Locate every blood parasite and identify its species.
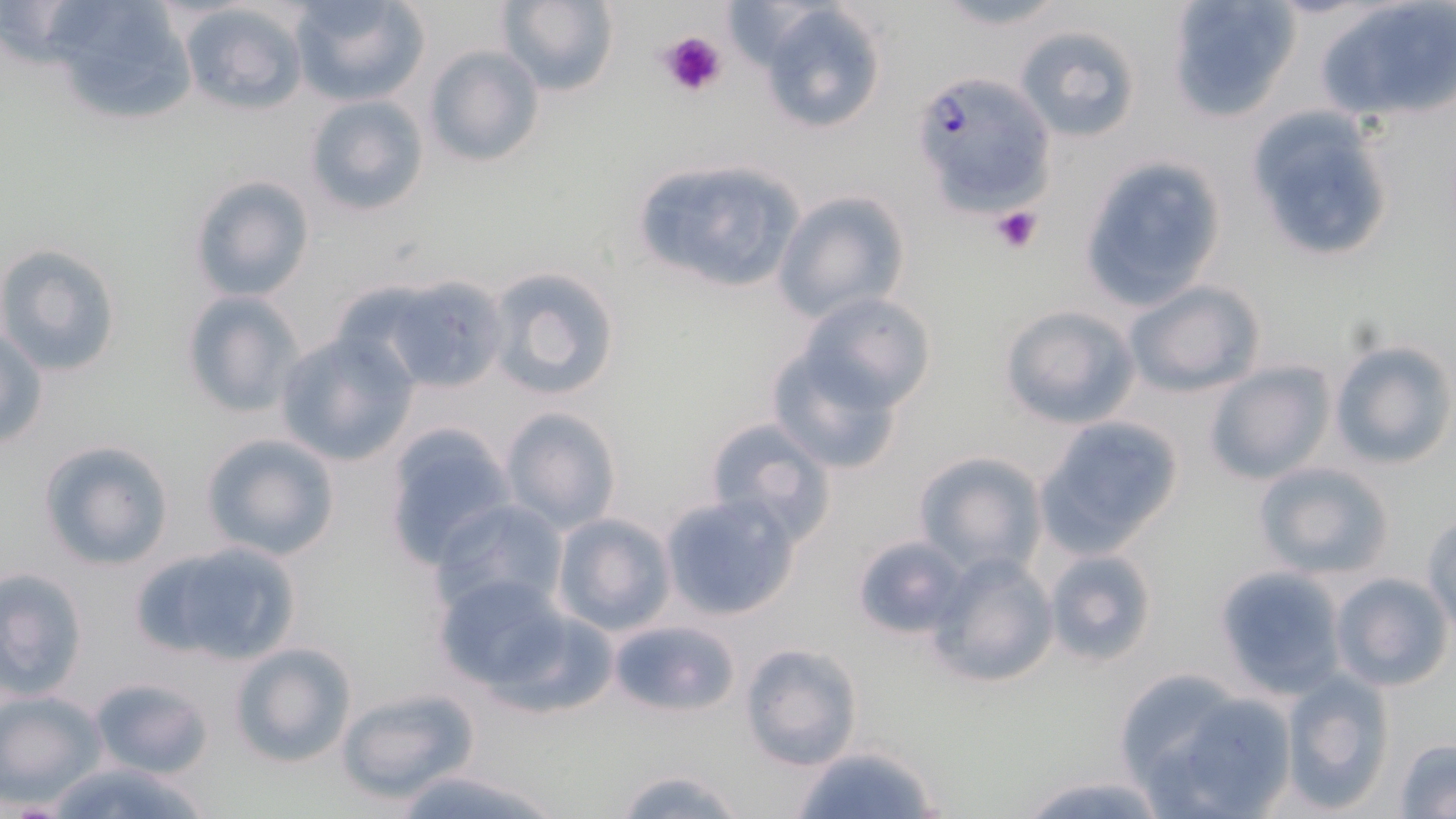
Approximate bounding boxes as [x1, y1, x2, y2] in pixels.
Plasmodium falciparum-infected red blood cells: [917, 79, 1060, 202].
No Plasmodium ovale, Plasmodium malariae, Plasmodium vivax, Babesia divergens, or Trypanosoma brucei observed.

slide-level diagnosis = Plasmodium falciparum
preparation = thin blood smear
platelet locations = approximate bounding boxes as [x1, y1, x2, y2] in pixels: [655, 30, 728, 102], [990, 205, 1045, 254]
modality = optical microscopy
image size = 1456×819 pixels
stain = May-Grünwald-Giemsa
field of view = one of a larger specimen
uninfected red blood cell locations = approximate bounding boxes as [x1, y1, x2, y2] in pixels: [40, 0, 206, 124], [287, 0, 429, 106], [496, 0, 619, 97], [928, 0, 1074, 31], [1166, 0, 1301, 122], [1319, 1, 1456, 123], [177, 2, 307, 115], [757, 3, 889, 135], [1014, 25, 1142, 142], [423, 44, 545, 168], [303, 94, 430, 217], [1243, 105, 1398, 265], [1080, 157, 1228, 306], [629, 158, 808, 297], [186, 174, 316, 302], [772, 189, 911, 325], [0, 242, 122, 378], [484, 266, 621, 401], [1124, 279, 1267, 397], [397, 280, 513, 399], [181, 290, 304, 418], [796, 292, 934, 411], [998, 304, 1140, 429], [1, 325, 48, 450], [275, 332, 417, 466], [768, 340, 910, 475], [1330, 340, 1453, 469], [1204, 361, 1335, 485], [498, 406, 622, 534], [702, 415, 837, 541], [1036, 417, 1184, 556], [382, 421, 518, 568], [200, 432, 339, 562], [37, 439, 174, 571], [913, 451, 1046, 574], [1252, 460, 1395, 580], [661, 493, 800, 621], [431, 498, 571, 615], [1423, 510, 1456, 629], [548, 514, 675, 636], [851, 535, 968, 640], [132, 538, 304, 669], [1042, 547, 1159, 668], [926, 551, 1059, 687], [1214, 566, 1346, 698], [1, 567, 88, 698], [1329, 571, 1453, 692], [433, 572, 584, 697], [609, 617, 737, 719], [738, 641, 863, 770], [228, 642, 357, 768], [1279, 670, 1395, 810], [89, 677, 215, 779], [336, 685, 482, 805], [1, 690, 106, 803], [1144, 690, 1298, 817], [1393, 737, 1456, 818], [787, 743, 942, 819], [46, 760, 217, 819], [610, 766, 750, 819], [394, 767, 565, 819], [1014, 769, 1169, 819]
magnification = 1000x